State the preparation type.
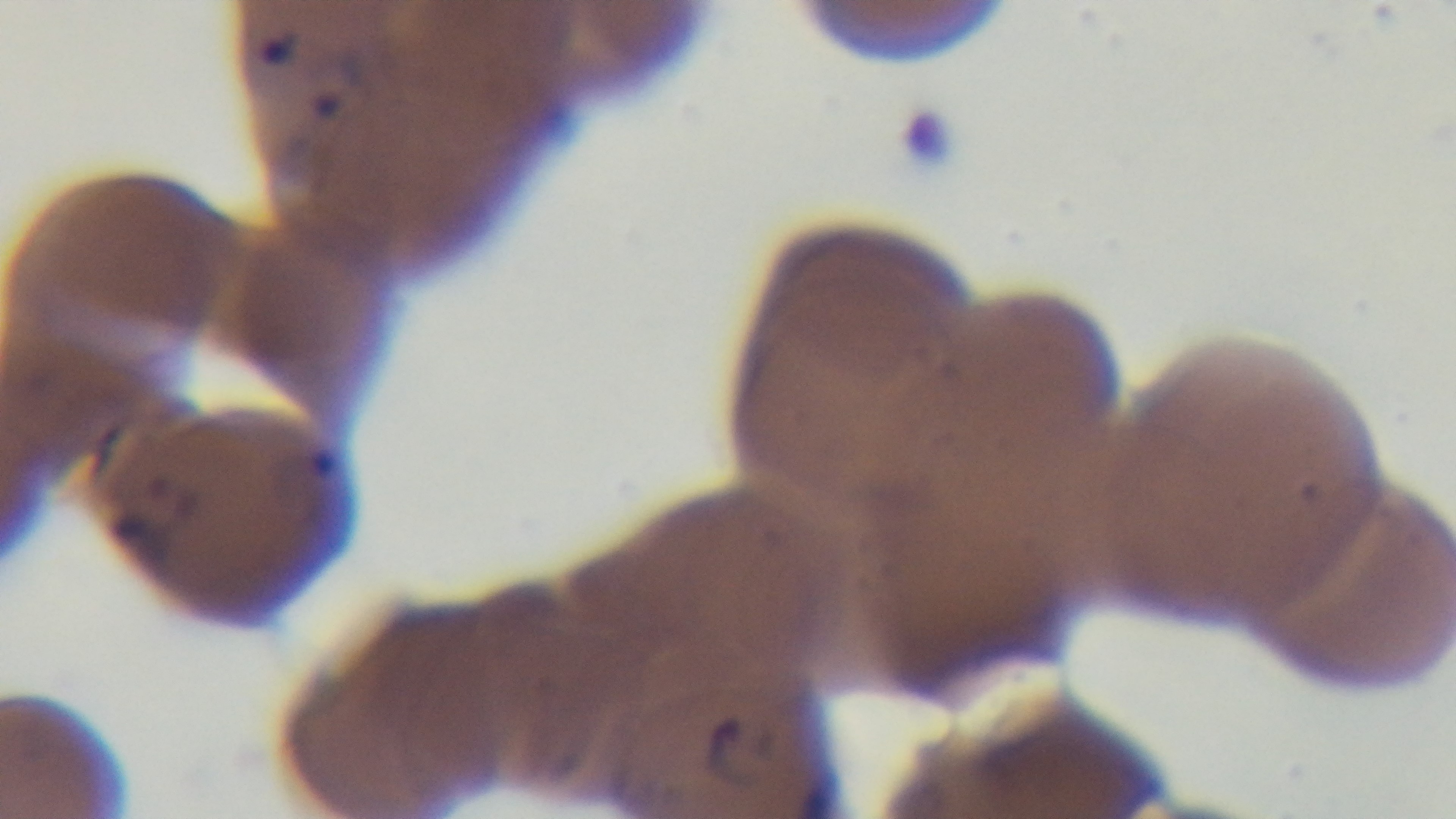
It is a thin blood film.

field_of_view: one from the slide
malaria_status: positive
stain: Giemsa
objective: 100x oil immersion
capture: mounted 4K digital camera
modality: light microscopy